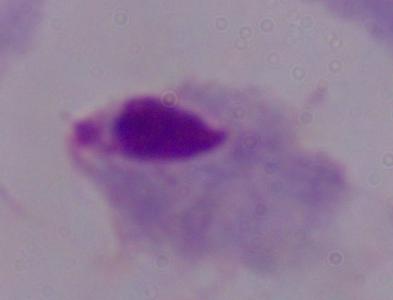

A trichomonad is shown. Photomicrograph. 1000x magnification.